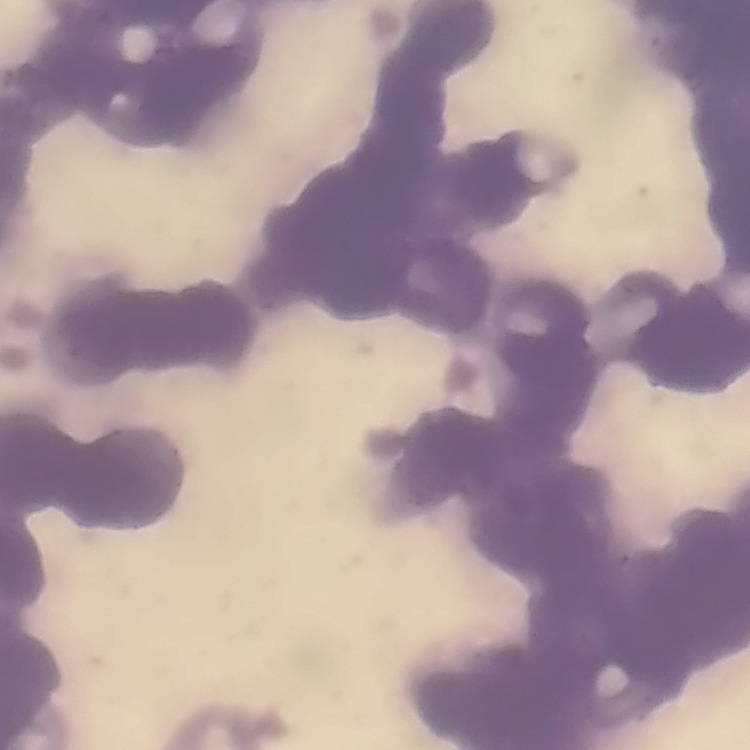
The erythrocytes exhibit rouleaux formation. Field's or Giemsa stain. Thin blood smear. One tile cut from a larger photomicrograph.